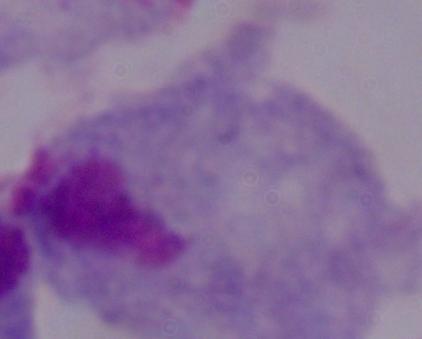
Photomicrograph. A trichomonad is shown. 1000x magnification.